Comment on the morphology of the erythrocytes.
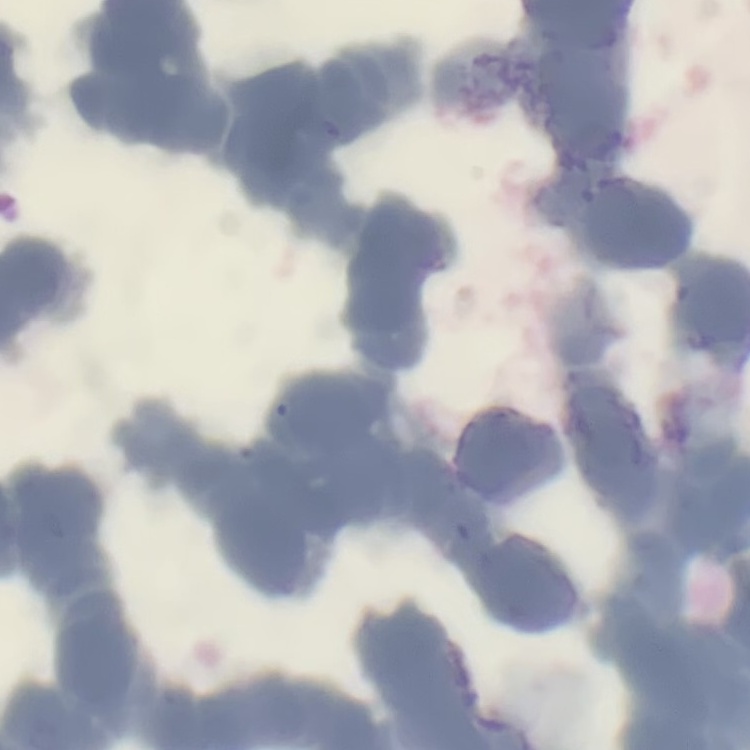

They show rouleaux formation.

Thin blood film. Square crop of a larger photomicrograph. Stained with either Field's or Giemsa.